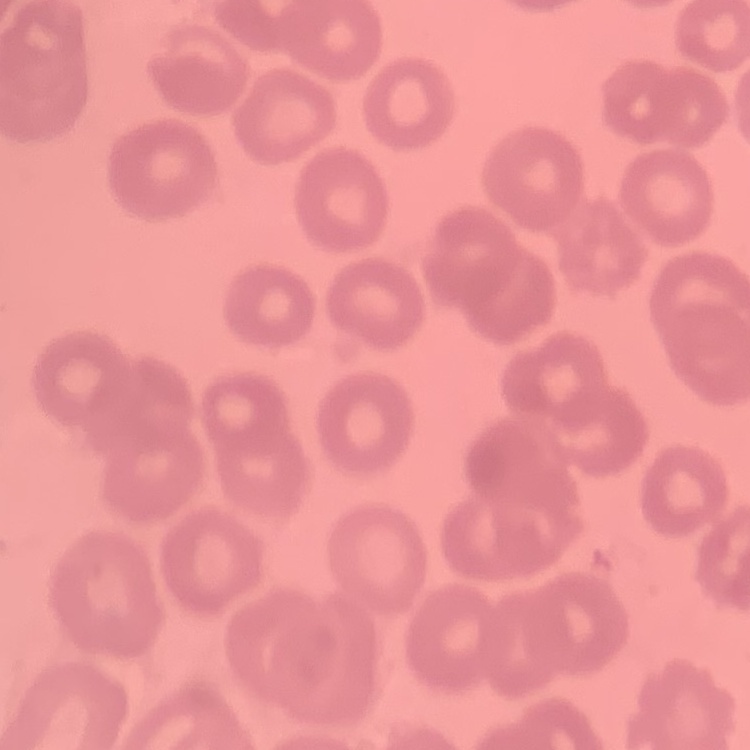 The erythrocytes show no rouleaux formation. Thin peripheral smear. Stained with either Field's or Giemsa. One tile cut from a larger photomicrograph.